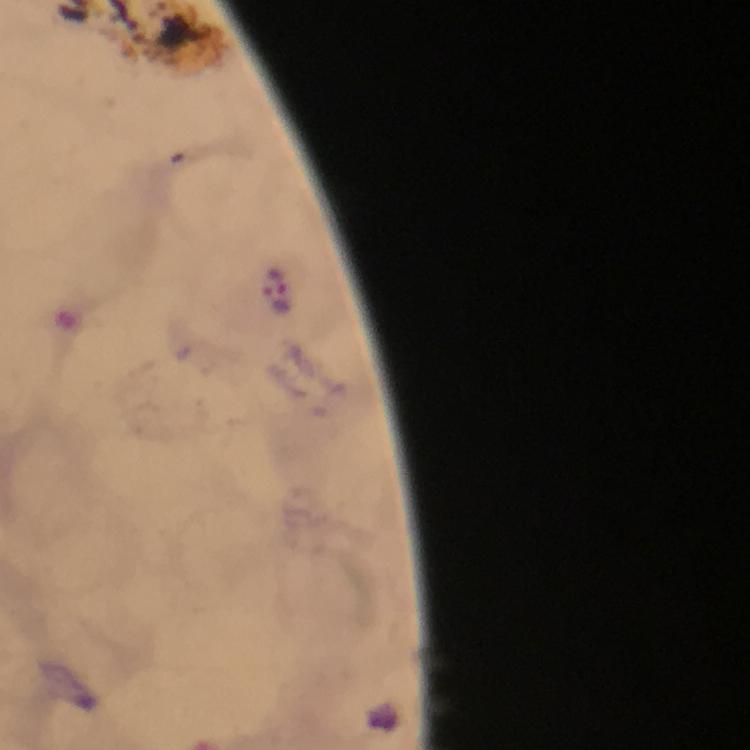

Approximate centers as {x, y} in pixels. Malaria parasite locations: {282, 282}, {275, 298}. Immersion oil was used. A crop from one field of view. Smartphone photograph taken through a microscope. From a malaria diagnostic workup. Giemsa-stained preparation. Thick smear. Image is 750×750 pixels. 100x magnification.